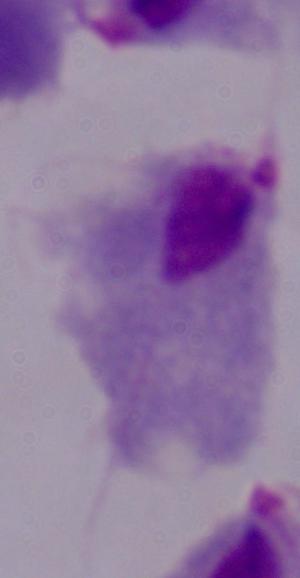
Summary:
  - Modality: photomicrograph
  - Magnification: 1000x
  - Identification: trichomonad